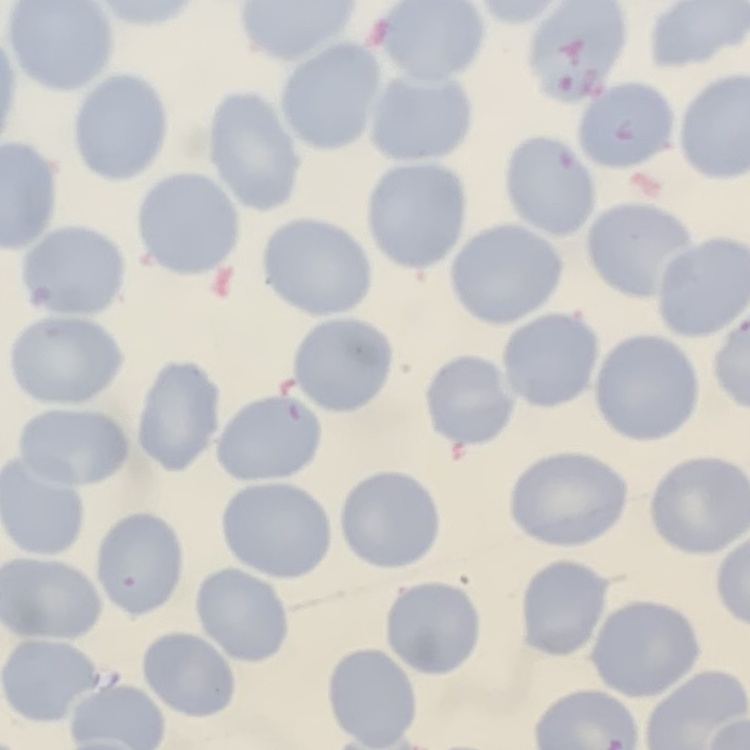

erythrocyte morphology = no rouleaux formation
preparation = thin peripheral smear
stain = Field's or Giemsa
image type = square crop of a larger photomicrograph